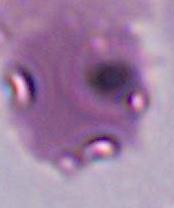
Summary:
  - Identification: Plasmodium
  - Modality: photomicrograph
  - Magnification: 400x or 1000x